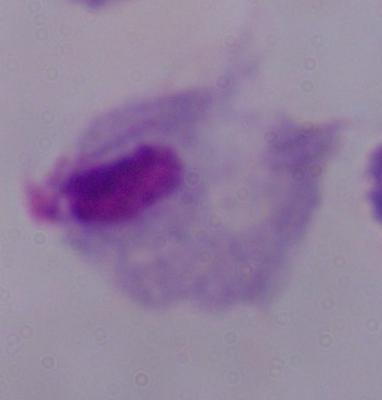

Summary:
  - Identification: trichomonad
  - Modality: photomicrograph
  - Magnification: 1000x